Classify this cell by malaria status.
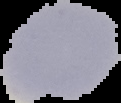
Uninfected.

image type = segmented cell region on a black background
preparation = thin blood film
image size = 121×103 pixels